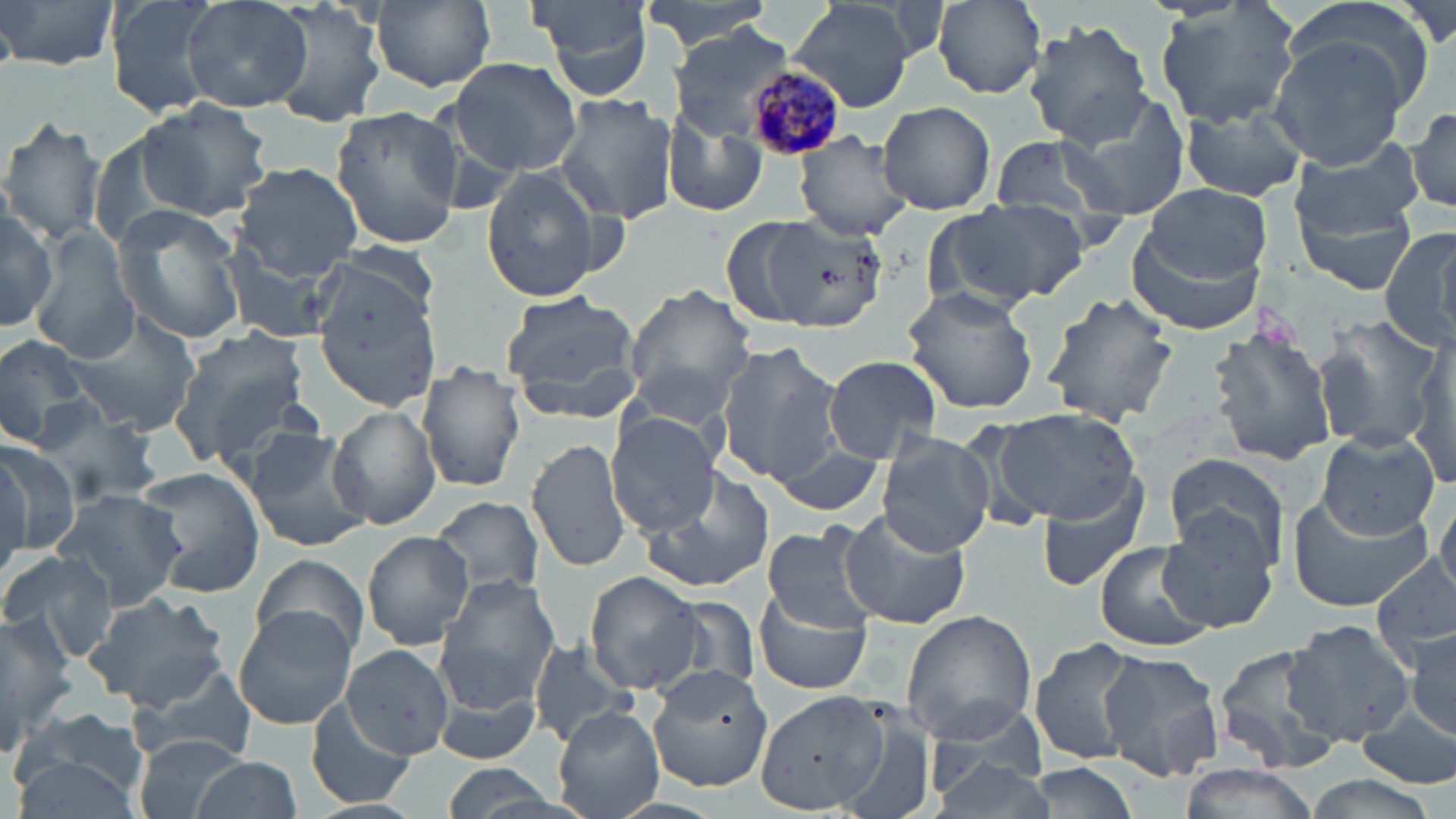
slide-level diagnosis = Plasmodium malariae
preparation = thin blood smear
modality = optical microscopy
stain = May-Grünwald-Giemsa
field of view = one of a larger specimen
Plasmodium malariae-infected red blood cell locations = approximate bounding boxes as named x1/y1/x2/y2 corners in pixels: (x1=746, y1=66, x2=847, y2=162)
image size = 1456×819 pixels
magnification = 1000x
uninfected red blood cell locations = approximate bounding boxes as named x1/y1/x2/y2 corners in pixels: (x1=3, y1=0, x2=121, y2=76), (x1=103, y1=0, x2=222, y2=116), (x1=181, y1=0, x2=314, y2=112), (x1=266, y1=0, x2=388, y2=127), (x1=371, y1=0, x2=498, y2=95), (x1=534, y1=0, x2=653, y2=100), (x1=641, y1=0, x2=778, y2=53), (x1=932, y1=0, x2=1045, y2=99), (x1=1283, y1=0, x2=1438, y2=115), (x1=787, y1=1, x2=924, y2=111), (x1=1152, y1=2, x2=1304, y2=130), (x1=1024, y1=21, x2=1156, y2=147), (x1=669, y1=25, x2=795, y2=139), (x1=1267, y1=38, x2=1410, y2=171), (x1=447, y1=59, x2=584, y2=174), (x1=1053, y1=87, x2=1194, y2=214), (x1=553, y1=95, x2=680, y2=223), (x1=137, y1=98, x2=274, y2=222), (x1=878, y1=100, x2=995, y2=213), (x1=1179, y1=103, x2=1308, y2=202), (x1=329, y1=104, x2=465, y2=252), (x1=1408, y1=104, x2=1456, y2=216), (x1=662, y1=111, x2=769, y2=220), (x1=0, y1=114, x2=107, y2=247), (x1=792, y1=132, x2=915, y2=242), (x1=990, y1=133, x2=1128, y2=227), (x1=1287, y1=134, x2=1426, y2=241), (x1=240, y1=140, x2=463, y2=275), (x1=230, y1=162, x2=365, y2=280), (x1=477, y1=166, x2=608, y2=301), (x1=1142, y1=183, x2=1275, y2=285), (x1=1294, y1=186, x2=1421, y2=298), (x1=952, y1=199, x2=1090, y2=304), (x1=0, y1=204, x2=57, y2=331), (x1=112, y1=204, x2=247, y2=347), (x1=757, y1=215, x2=885, y2=333), (x1=721, y1=217, x2=815, y2=327), (x1=1379, y1=224, x2=1456, y2=354), (x1=1124, y1=225, x2=1267, y2=337), (x1=32, y1=227, x2=142, y2=364), (x1=219, y1=244, x2=347, y2=346), (x1=312, y1=276, x2=444, y2=410), (x1=621, y1=284, x2=760, y2=421), (x1=902, y1=286, x2=1039, y2=415), (x1=1043, y1=291, x2=1179, y2=428), (x1=500, y1=293, x2=644, y2=422), (x1=62, y1=311, x2=204, y2=438), (x1=1311, y1=311, x2=1445, y2=452), (x1=1207, y1=325, x2=1339, y2=467), (x1=170, y1=327, x2=313, y2=475), (x1=0, y1=332, x2=93, y2=450), (x1=1406, y1=338, x2=1455, y2=490), (x1=716, y1=341, x2=844, y2=481), (x1=822, y1=355, x2=942, y2=462), (x1=419, y1=360, x2=526, y2=493), (x1=22, y1=396, x2=161, y2=509), (x1=329, y1=404, x2=441, y2=531), (x1=994, y1=408, x2=1143, y2=526), (x1=607, y1=410, x2=723, y2=534), (x1=245, y1=429, x2=371, y2=552), (x1=1316, y1=429, x2=1442, y2=542), (x1=876, y1=431, x2=994, y2=557), (x1=527, y1=434, x2=629, y2=575), (x1=0, y1=437, x2=80, y2=562), (x1=772, y1=442, x2=887, y2=514), (x1=1164, y1=451, x2=1289, y2=568), (x1=137, y1=465, x2=263, y2=597), (x1=639, y1=466, x2=775, y2=595), (x1=1035, y1=467, x2=1156, y2=592), (x1=52, y1=487, x2=187, y2=610), (x1=1434, y1=493, x2=1455, y2=599), (x1=430, y1=496, x2=544, y2=604), (x1=1286, y1=497, x2=1437, y2=613), (x1=1156, y1=507, x2=1279, y2=634), (x1=840, y1=509, x2=970, y2=629), (x1=761, y1=522, x2=881, y2=632), (x1=364, y1=531, x2=472, y2=649), (x1=1094, y1=540, x2=1212, y2=653), (x1=0, y1=549, x2=119, y2=662), (x1=1374, y1=552, x2=1455, y2=663), (x1=251, y1=553, x2=369, y2=660), (x1=585, y1=572, x2=703, y2=693), (x1=434, y1=578, x2=560, y2=709), (x1=755, y1=584, x2=872, y2=693), (x1=84, y1=592, x2=229, y2=713), (x1=660, y1=594, x2=763, y2=698), (x1=235, y1=608, x2=355, y2=728), (x1=900, y1=610, x2=1038, y2=743), (x1=0, y1=611, x2=74, y2=761), (x1=1283, y1=620, x2=1416, y2=746), (x1=1404, y1=621, x2=1456, y2=745), (x1=1028, y1=637, x2=1143, y2=764), (x1=528, y1=642, x2=635, y2=750), (x1=1213, y1=643, x2=1349, y2=775), (x1=341, y1=644, x2=454, y2=759), (x1=1098, y1=650, x2=1224, y2=781), (x1=124, y1=662, x2=258, y2=769), (x1=645, y1=662, x2=776, y2=794), (x1=434, y1=686, x2=540, y2=765), (x1=755, y1=688, x2=889, y2=813), (x1=304, y1=701, x2=413, y2=808), (x1=828, y1=701, x2=941, y2=819), (x1=554, y1=703, x2=664, y2=819), (x1=924, y1=703, x2=1050, y2=800), (x1=8, y1=706, x2=150, y2=814), (x1=1358, y1=708, x2=1455, y2=790), (x1=130, y1=733, x2=255, y2=819), (x1=926, y1=757, x2=1060, y2=818), (x1=193, y1=758, x2=300, y2=817), (x1=1019, y1=761, x2=1144, y2=819), (x1=432, y1=763, x2=575, y2=819), (x1=1174, y1=768, x2=1320, y2=819), (x1=1301, y1=774, x2=1443, y2=819)